Give the position of every leukocyte visible.
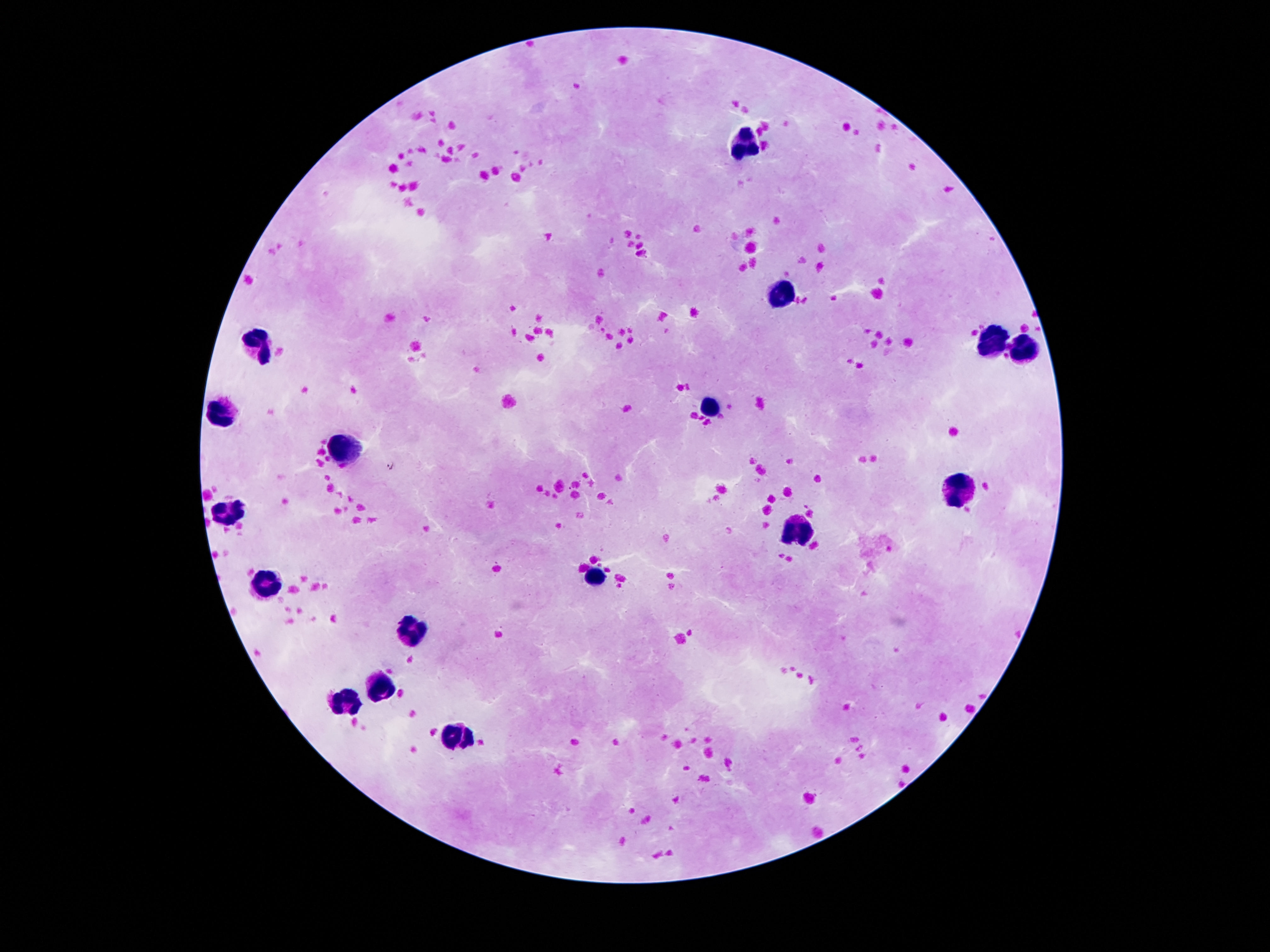

Approximate centers as {x, y} in pixels.
Leukocytes: {744, 139}, {786, 288}, {993, 344}, {261, 345}, {1024, 353}, {707, 405}, {221, 412}, {345, 449}, {954, 492}, {229, 516}, {797, 528}, {597, 577}, {268, 580}, {415, 629}, {382, 685}, {347, 700}, {457, 738}.

magnification: 100x
stain: Giemsa
patient_malaria_status: negative
image_size: 1270×952 pixels
preparation: thick blood smear
capture: smartphone camera through the microscope eyepiece
field_of_view: one from this slide